Identify the cell.
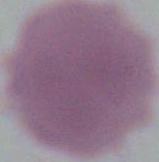

An erythrocyte.

modality = micrograph
magnification = 1000x